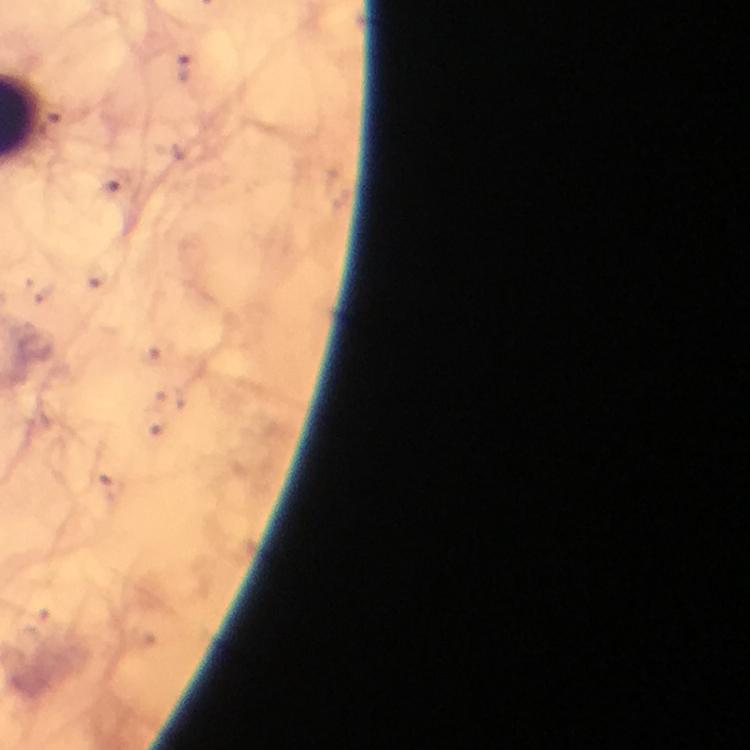

magnification = 100x
stain = Giemsa
context = from a malaria diagnostic workup
cropped from = one field of view
preparation = thick blood smear
immersion oil = used
malaria parasite locations = approximate centers as {x, y} in pixels: {184, 67}, {119, 184}
image size = 750×750 pixels
capture = smartphone camera through the microscope